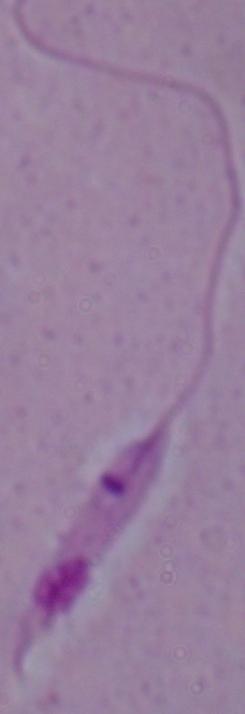

modality = photomicrograph
magnification = 1000x
identification = Leishmania